Report the malaria status of this cell.
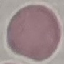

Uninfected.

Thin blood film. Automatically extracted cell patch, resized to 64 × 64 pixels. Acquired by smartphone through the microscope eyepiece. Giemsa stain.